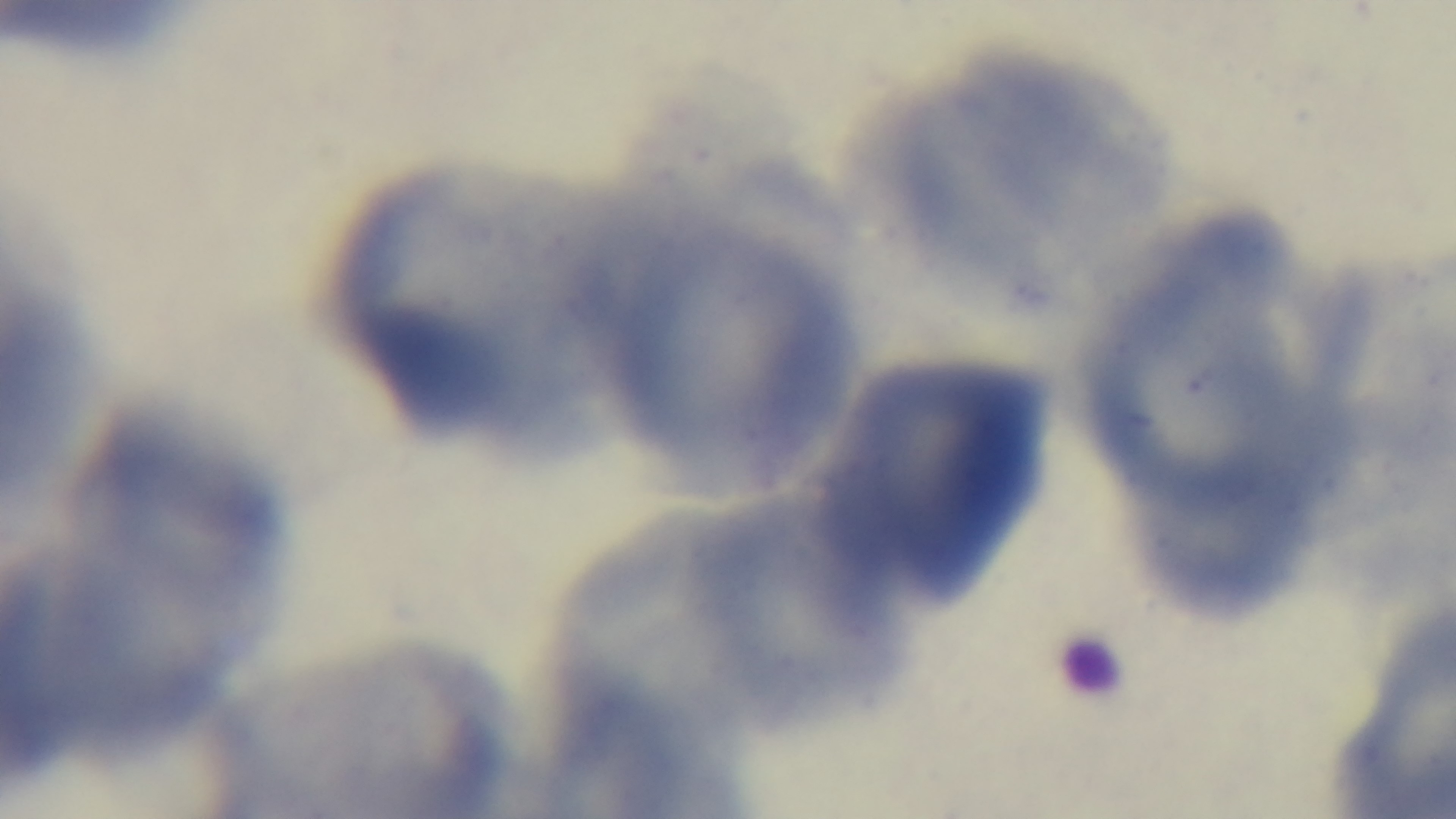
Preparation: thin smear. Photomicrograph. Captured with a mounted 4K digital camera. Malaria status: negative. Giemsa stain. Oil-immersion objective, 100x. Single field of view.